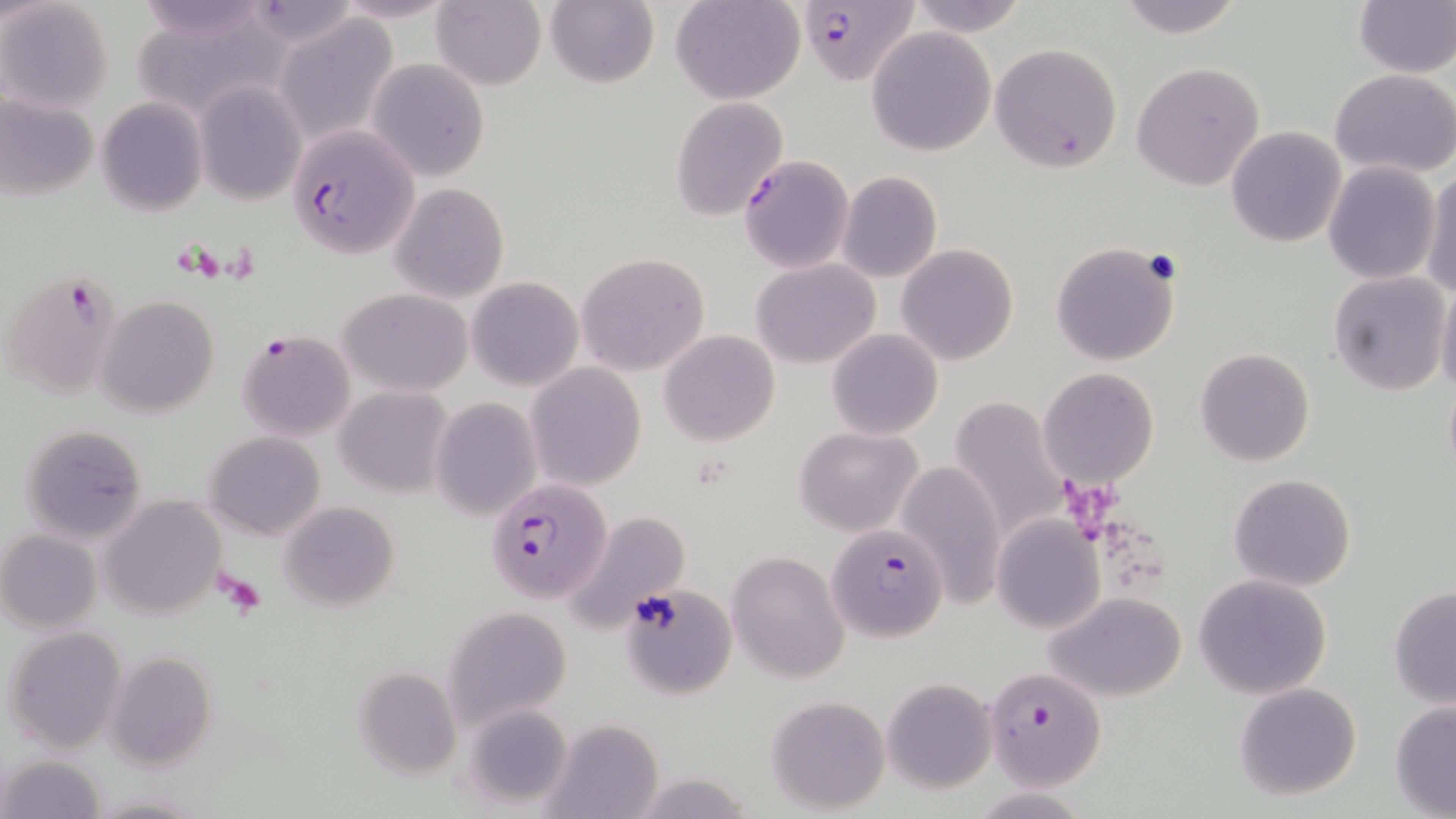

slide-level diagnosis = Plasmodium falciparum
field of view = one of a larger specimen
Plasmodium falciparum-infected red blood cell locations = approximate bounding boxes as [x1, y1, x2, y2] in pixels: [794, 0, 916, 85], [291, 125, 421, 260], [738, 154, 853, 274], [3, 267, 123, 399], [236, 329, 358, 443], [481, 480, 617, 609], [830, 527, 949, 641], [983, 664, 1106, 789]
modality = optical microscopy
preparation = thin blood smear
magnification = 1000x
uninfected red blood cell locations = approximate bounding boxes as [x1, y1, x2, y2] in pixels: [1, 0, 114, 114], [134, 0, 272, 45], [328, 0, 460, 24], [543, 0, 659, 89], [672, 0, 804, 104], [906, 0, 1030, 38], [1111, 0, 1246, 38], [1352, 0, 1456, 77], [431, 1, 546, 90], [275, 13, 400, 144], [866, 26, 997, 156], [991, 42, 1126, 174], [368, 58, 489, 182], [1132, 61, 1266, 192], [1330, 68, 1456, 177], [192, 82, 306, 203], [1, 94, 98, 199], [670, 96, 789, 222], [96, 97, 208, 215], [1226, 127, 1346, 247], [1323, 159, 1440, 285], [1421, 165, 1456, 301], [837, 172, 943, 282], [389, 183, 509, 302], [896, 243, 1018, 366], [1051, 243, 1180, 366], [576, 252, 710, 375], [751, 258, 879, 369], [1329, 272, 1450, 394], [467, 278, 583, 390], [1436, 282, 1456, 403], [339, 287, 473, 396], [97, 296, 219, 418], [660, 329, 780, 445], [827, 329, 942, 440], [1195, 348, 1314, 466], [526, 363, 647, 491], [1038, 367, 1159, 489], [335, 387, 453, 496], [947, 396, 1067, 539], [431, 398, 541, 520], [18, 422, 149, 542], [795, 426, 922, 535], [204, 431, 326, 542], [897, 460, 1005, 609], [1228, 472, 1356, 592], [101, 496, 226, 622], [279, 500, 400, 611], [563, 510, 690, 635], [990, 515, 1104, 634], [0, 530, 102, 632], [727, 550, 850, 681], [1193, 574, 1332, 700], [621, 582, 736, 698], [1388, 586, 1456, 709], [1046, 591, 1188, 700], [441, 608, 571, 729], [3, 626, 128, 754], [106, 651, 217, 771], [354, 666, 463, 780], [882, 677, 998, 793], [1234, 682, 1363, 801], [767, 694, 891, 812], [1389, 701, 1456, 818], [460, 703, 575, 811], [542, 719, 665, 819], [1, 753, 106, 819], [89, 791, 203, 818]
image size = 1456×819 pixels
stain = May-Grünwald-Giemsa